Assess this cell for malaria.
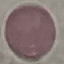
It is uninfected.

preparation = thin blood film
image type = cell patch, automatically extracted from a larger field of view and resized to 64 × 64 pixels
capture = smartphone through the microscope eyepiece
stain = Giemsa